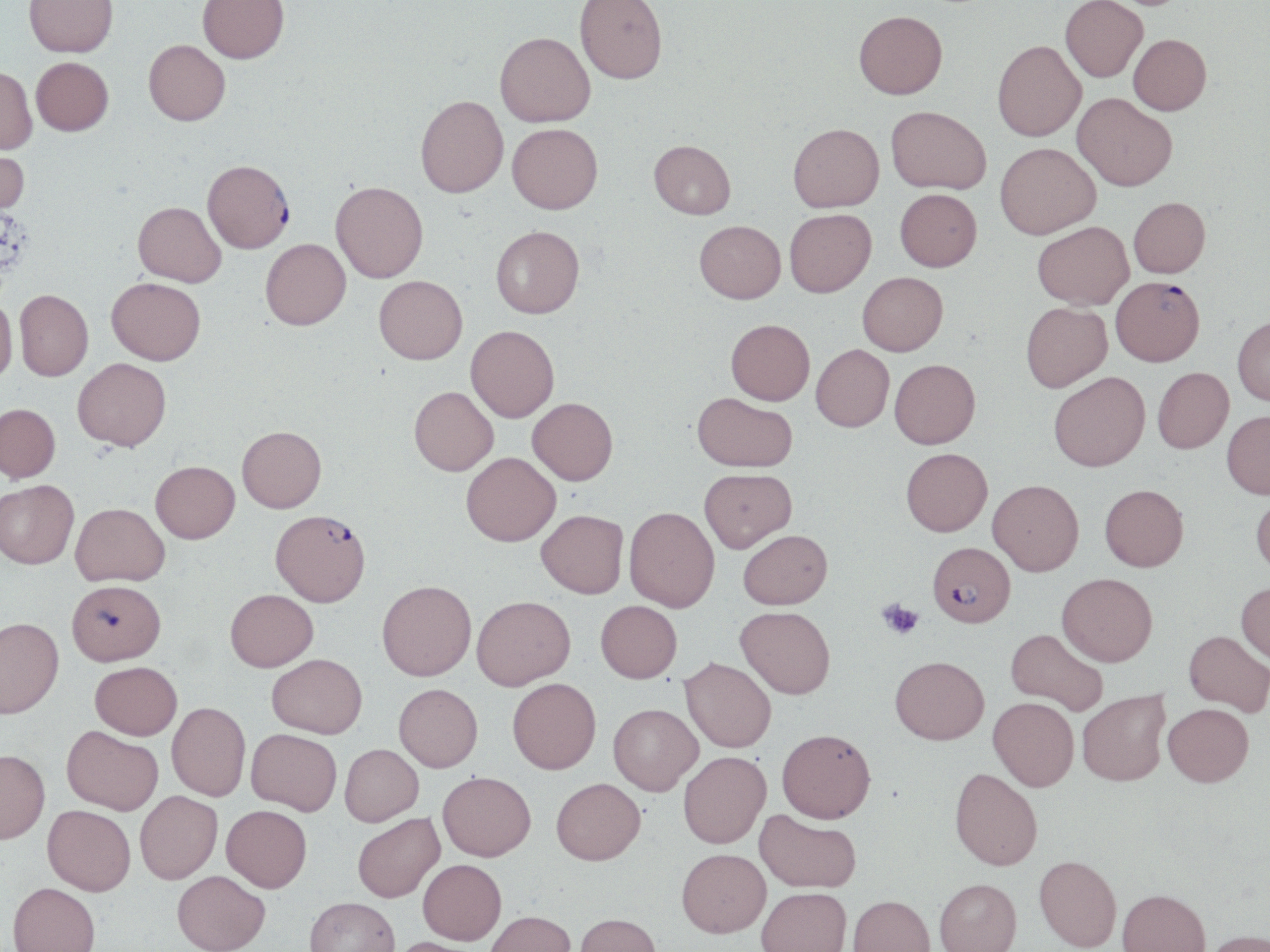 Approximate bounding boxes as named x1/y1/x2/y2 corners in pixels. Platelet locations: (x1=878, y1=599, x2=923, y2=640). Uninfected red blood cell locations: (x1=24, y1=0, x2=118, y2=58), (x1=197, y1=0, x2=289, y2=67), (x1=575, y1=0, x2=667, y2=88), (x1=1060, y1=0, x2=1147, y2=85), (x1=1104, y1=0, x2=1194, y2=14), (x1=854, y1=16, x2=947, y2=104), (x1=494, y1=35, x2=595, y2=130), (x1=1128, y1=37, x2=1212, y2=119), (x1=143, y1=41, x2=230, y2=128), (x1=992, y1=44, x2=1086, y2=145), (x1=31, y1=57, x2=113, y2=136), (x1=0, y1=67, x2=37, y2=155), (x1=415, y1=96, x2=508, y2=199), (x1=1072, y1=96, x2=1176, y2=195), (x1=885, y1=109, x2=990, y2=197), (x1=507, y1=126, x2=603, y2=217), (x1=788, y1=128, x2=884, y2=216), (x1=0, y1=144, x2=29, y2=217), (x1=648, y1=144, x2=736, y2=222), (x1=995, y1=146, x2=1100, y2=243), (x1=330, y1=180, x2=428, y2=282), (x1=895, y1=193, x2=982, y2=274), (x1=133, y1=201, x2=226, y2=286), (x1=1129, y1=201, x2=1210, y2=282), (x1=785, y1=212, x2=877, y2=300), (x1=694, y1=224, x2=785, y2=307), (x1=491, y1=225, x2=584, y2=318), (x1=1033, y1=225, x2=1133, y2=312), (x1=260, y1=238, x2=351, y2=329), (x1=857, y1=274, x2=948, y2=358), (x1=374, y1=275, x2=467, y2=364), (x1=106, y1=276, x2=206, y2=364), (x1=14, y1=289, x2=93, y2=380), (x1=0, y1=296, x2=17, y2=384), (x1=1021, y1=304, x2=1112, y2=393), (x1=1232, y1=317, x2=1270, y2=408), (x1=725, y1=320, x2=814, y2=407), (x1=466, y1=325, x2=559, y2=422), (x1=811, y1=345, x2=894, y2=432), (x1=73, y1=358, x2=171, y2=451), (x1=890, y1=359, x2=980, y2=448), (x1=1153, y1=369, x2=1234, y2=454), (x1=1049, y1=372, x2=1150, y2=471), (x1=409, y1=386, x2=498, y2=475), (x1=692, y1=393, x2=797, y2=473), (x1=527, y1=397, x2=617, y2=484), (x1=0, y1=403, x2=60, y2=482), (x1=1222, y1=411, x2=1270, y2=499), (x1=237, y1=425, x2=326, y2=512), (x1=901, y1=447, x2=993, y2=535), (x1=462, y1=452, x2=560, y2=545), (x1=150, y1=460, x2=239, y2=543), (x1=699, y1=467, x2=797, y2=552), (x1=0, y1=479, x2=79, y2=568), (x1=988, y1=479, x2=1084, y2=575), (x1=1100, y1=484, x2=1189, y2=571), (x1=1251, y1=491, x2=1270, y2=579), (x1=71, y1=502, x2=169, y2=586), (x1=625, y1=507, x2=719, y2=612), (x1=536, y1=509, x2=628, y2=598), (x1=738, y1=529, x2=832, y2=609), (x1=1057, y1=573, x2=1157, y2=665), (x1=377, y1=580, x2=476, y2=680), (x1=1236, y1=582, x2=1270, y2=665), (x1=225, y1=588, x2=318, y2=671), (x1=472, y1=595, x2=575, y2=689), (x1=595, y1=600, x2=682, y2=682), (x1=735, y1=606, x2=835, y2=698), (x1=0, y1=617, x2=64, y2=718), (x1=1006, y1=628, x2=1107, y2=715), (x1=1184, y1=630, x2=1269, y2=714), (x1=267, y1=653, x2=367, y2=738), (x1=680, y1=657, x2=776, y2=752), (x1=890, y1=657, x2=989, y2=743), (x1=90, y1=661, x2=182, y2=740), (x1=507, y1=677, x2=601, y2=773), (x1=394, y1=683, x2=482, y2=772), (x1=1077, y1=689, x2=1170, y2=786), (x1=988, y1=697, x2=1079, y2=791), (x1=167, y1=702, x2=251, y2=799), (x1=608, y1=703, x2=703, y2=795), (x1=1163, y1=703, x2=1254, y2=786), (x1=62, y1=725, x2=163, y2=815), (x1=247, y1=728, x2=342, y2=815), (x1=777, y1=728, x2=876, y2=822), (x1=340, y1=743, x2=423, y2=826), (x1=0, y1=749, x2=50, y2=844), (x1=678, y1=751, x2=771, y2=848), (x1=949, y1=768, x2=1042, y2=870), (x1=438, y1=771, x2=536, y2=860), (x1=551, y1=778, x2=645, y2=865), (x1=135, y1=790, x2=222, y2=883), (x1=43, y1=804, x2=136, y2=895), (x1=222, y1=804, x2=312, y2=891), (x1=755, y1=810, x2=861, y2=892), (x1=352, y1=812, x2=444, y2=902), (x1=677, y1=848, x2=771, y2=937), (x1=1034, y1=854, x2=1121, y2=951), (x1=418, y1=858, x2=506, y2=944), (x1=173, y1=870, x2=270, y2=952), (x1=935, y1=878, x2=1021, y2=952), (x1=8, y1=882, x2=100, y2=952), (x1=757, y1=887, x2=851, y2=952), (x1=1118, y1=888, x2=1210, y2=952), (x1=848, y1=895, x2=935, y2=952), (x1=305, y1=896, x2=399, y2=952), (x1=486, y1=910, x2=576, y2=952), (x1=574, y1=913, x2=662, y2=952), (x1=1203, y1=929, x2=1270, y2=952), (x1=386, y1=936, x2=484, y2=952). Plasmodium falciparum-infected red blood cell locations: (x1=202, y1=161, x2=294, y2=254), (x1=1111, y1=280, x2=1204, y2=370), (x1=270, y1=509, x2=370, y2=606), (x1=927, y1=541, x2=1015, y2=627), (x1=67, y1=579, x2=166, y2=665). Slide-level diagnosis: Plasmodium falciparum. Light microscopy. One field of a larger specimen. Image is 1270×952 pixels. Captured at 1000x magnification. May-Grünwald-Giemsa-stained preparation. Thin blood film.